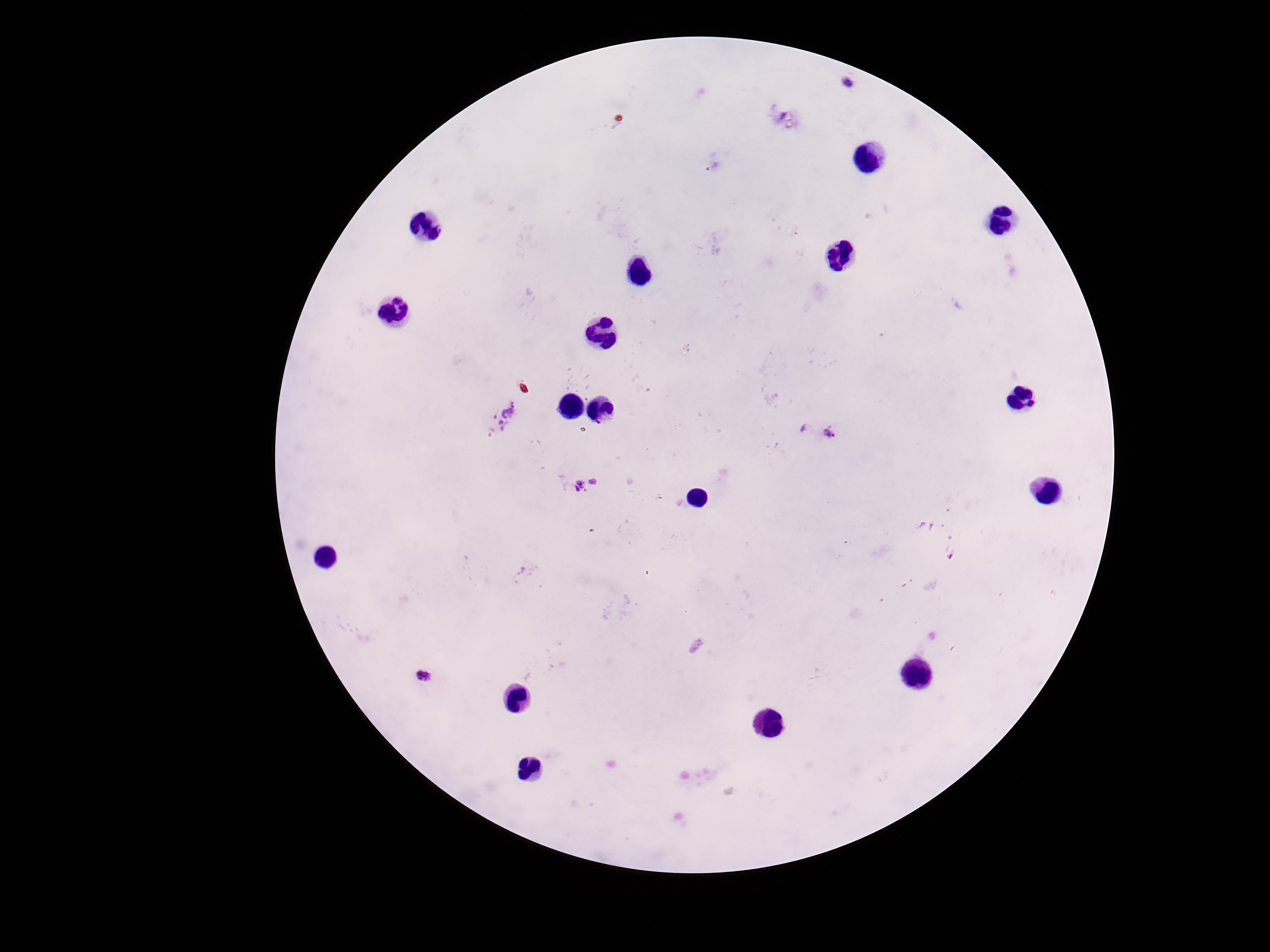
magnification: 100x
patient_malaria_status: positive
plasmodium_parasite_locations: 'approximate centers as (x, y) in pixels: (851, 84), (505, 416), (832, 434), (585, 487), (426, 677)'
image_size: 1270×952 pixels
field_of_view: single
preparation: thick blood smear
capture: smartphone camera through the microscope eyepiece
stain: Giemsa